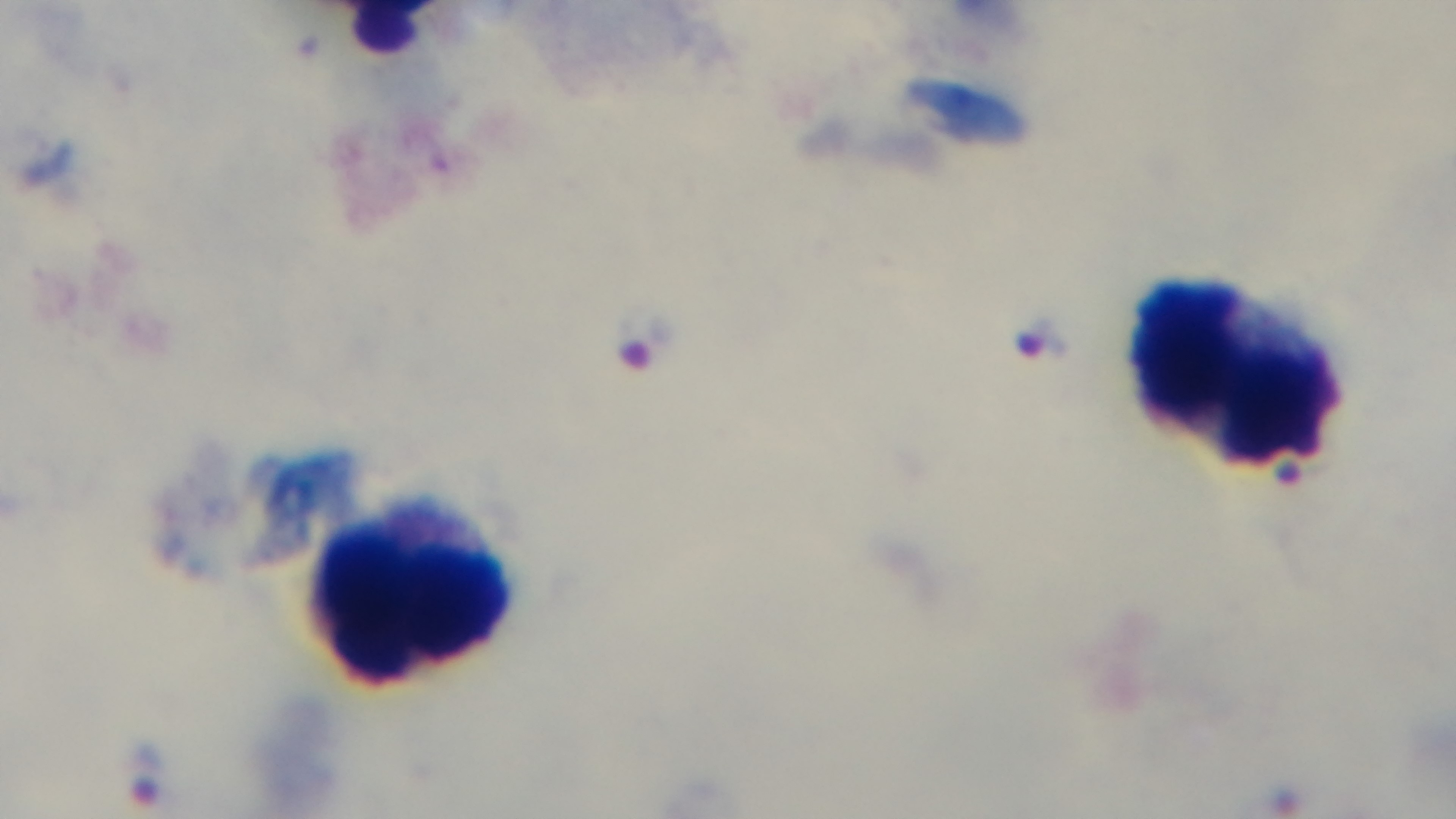
modality = light microscopy
field of view = one from the slide
capture = mounted 4K digital camera
preparation = thick smear
malaria status = infected
stain = Giemsa
objective = 100x oil immersion